Assess the morphology of the red blood cells.
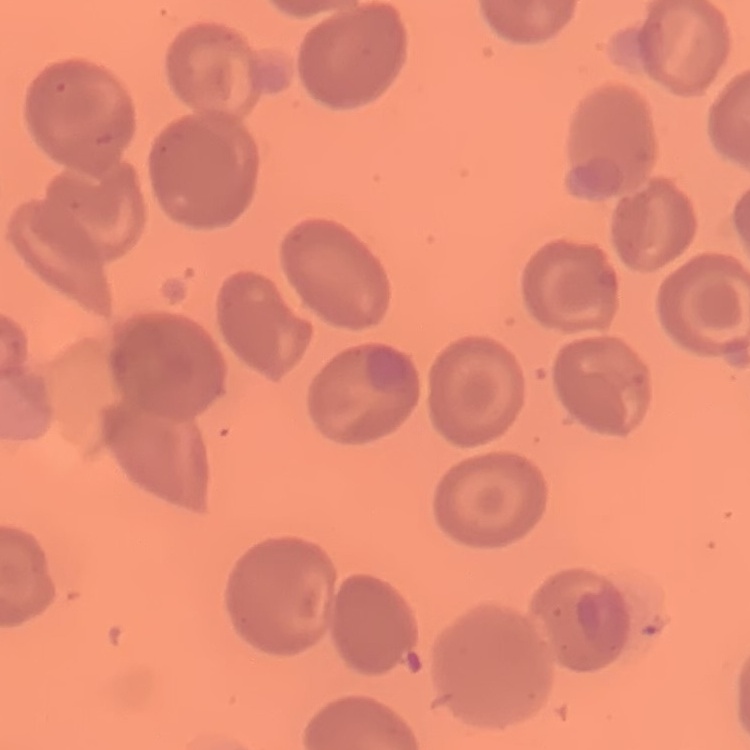

They show no rouleaux formation.

Summary:
  - Stain: Field's or Giemsa
  - Image type: one tile cut from a larger photomicrograph
  - Preparation: thin peripheral smear